Assess this cell for malaria.
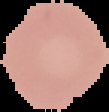
It is uninfected.

image_type: segmented cell region on a black background
image_size: 109×112 pixels
preparation: thin blood smear